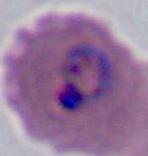

{
  "modality": "photomicrograph",
  "magnification": "400x or 1000x",
  "identification": "Plasmodium"
}